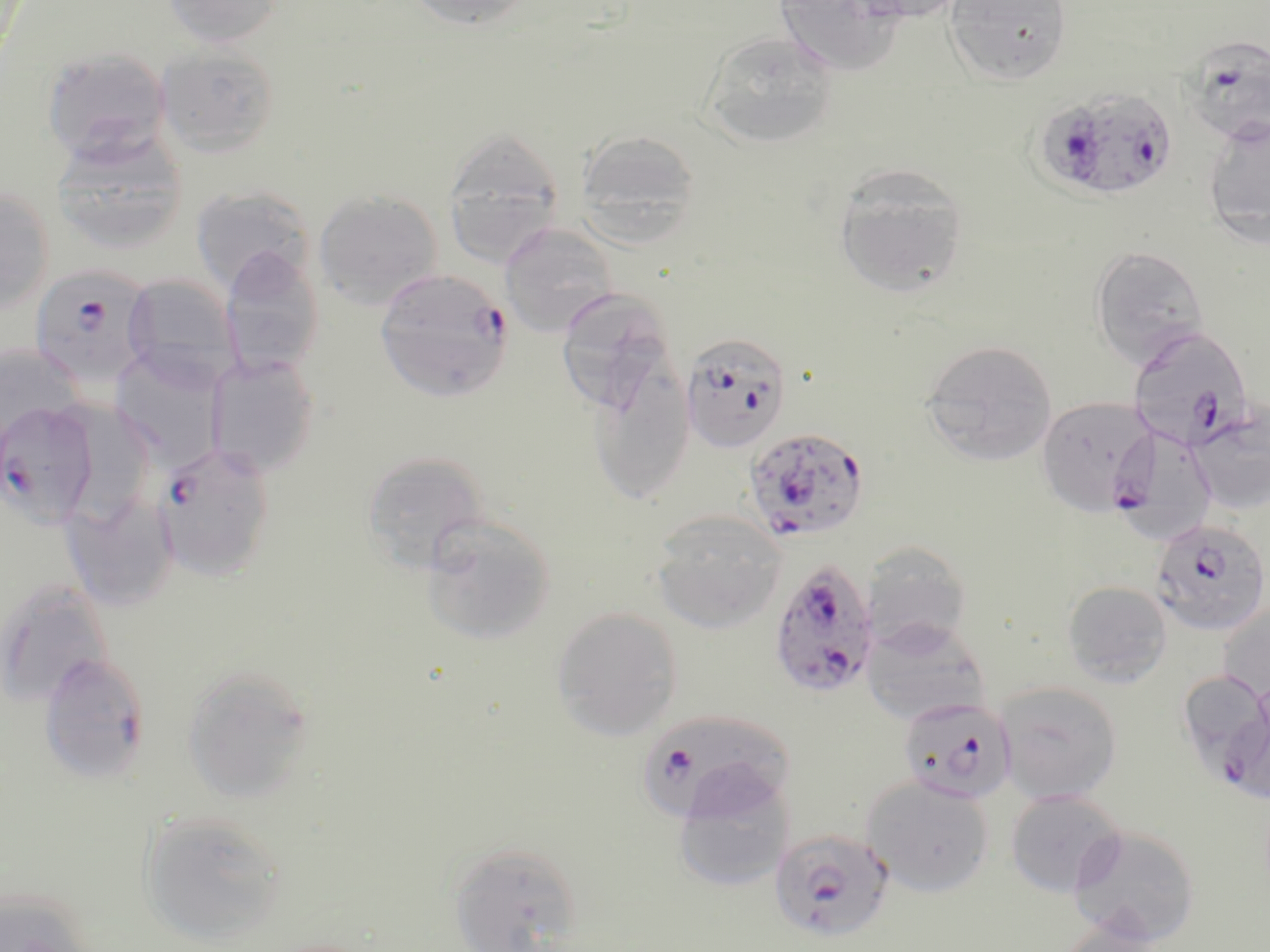

{
  "slide_level_diagnosis": "Plasmodium falciparum",
  "image_size": "1270×952 pixels",
  "modality": "light microscopy",
  "uninfected_red_blood_cell_locations_subset": "approximate bounding boxes as (x1,y1)-(x2,y2) corner pairs in pixels: (163,0)-(283,49), (403,0)-(537,30), (774,0)-(907,76), (840,0)-(973,23), (944,0)-(1073,85), (700,29)-(840,150), (155,44)-(280,158), (41,46)-(172,168), (1202,114)-(1270,246), (442,125)-(564,268), (50,128)-(189,256), (574,129)-(702,242), (832,163)-(968,299), (0,186)-(56,314), (191,186)-(314,294), (313,189)-(443,311), (499,223)-(617,336), (1089,244)-(1210,369), (218,247)-(325,380), (121,274)-(242,392), (555,290)-(679,413), (921,339)-(1057,466), (0,342)-(88,449), (110,348)-(226,470), (205,355)-(320,478), (588,365)-(695,505), (1186,405)-(1270,517), (361,450)-(492,572), (61,495)-(180,612), (650,510)-(786,634), (419,514)-(556,646), (863,542)-(973,654), (0,576)-(114,708), (1062,581)-(1172,687), (1218,601)-(1270,705), (551,606)-(683,741), (861,619)-(991,726), (182,665)-(314,804), (994,681)-(1123,804), (672,772)-(794,892), (862,775)-(995,897), (1005,789)-(1126,898), (140,809)-(286,945), (1067,823)-(1201,947), (448,840)-(583,951), (0,888)-(97,952), (1055,921)-(1168,952)",
  "magnification": "1000x",
  "plasmodium_falciparum_infected_red_blood_cell_locations_subset": "approximate bounding boxes as (x1,y1)-(x2,y2) corner pairs in pixels: (1180,34)-(1270,148), (1034,85)-(1179,202), (375,268)-(513,403), (1126,327)-(1257,452), (679,332)-(792,453), (1036,396)-(1156,516), (0,399)-(100,528), (1108,422)-(1219,543), (743,425)-(871,543), (152,441)-(275,582), (1150,518)-(1270,637), (770,556)-(881,701), (38,653)-(151,784), (1218,696)-(1270,803), (898,697)-(1016,804), (637,709)-(796,823), (769,827)-(894,943)",
  "preparation": "thin blood smear",
  "stain": "May-Grünwald-Giemsa",
  "field_of_view": "single"
}